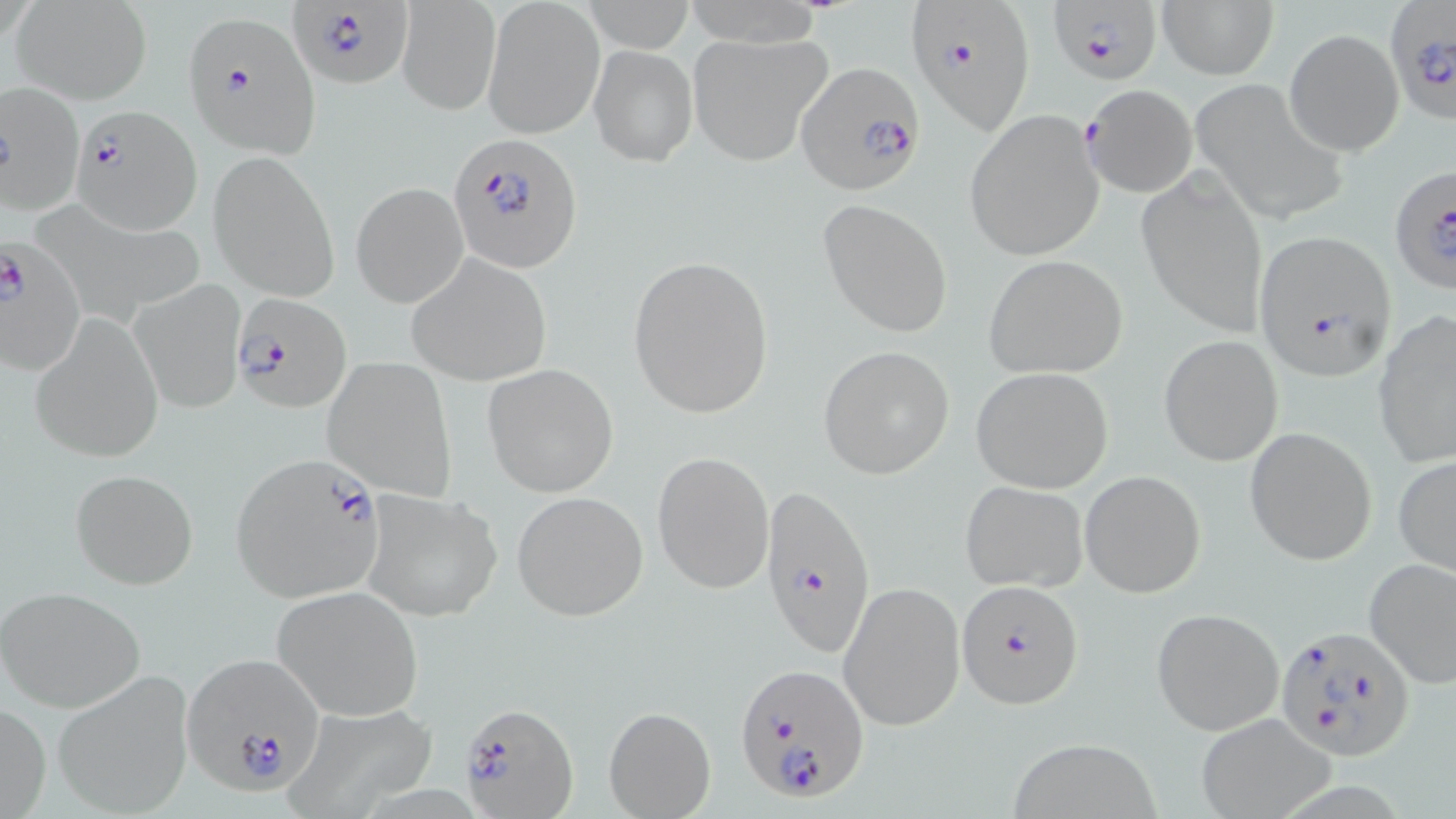 Approximate bounding boxes as (x1,y1)-(x2,y2) corner pairs in pixels. Plasmodium falciparum-infected red blood cell locations: (287,0)-(414,88), (902,0)-(1037,134), (1050,1)-(1161,84), (1384,3)-(1455,126), (182,10)-(320,157), (797,62)-(924,194), (0,82)-(84,214), (1081,84)-(1194,196), (70,106)-(200,232), (449,133)-(584,272), (1388,166)-(1456,295), (1251,230)-(1397,379), (0,234)-(86,375), (231,291)-(352,413), (228,454)-(389,603), (759,480)-(875,658), (957,582)-(1084,709), (1273,626)-(1418,760), (180,654)-(327,796), (735,663)-(868,802), (457,701)-(578,818). Uninfected red blood cell locations: (483,0)-(604,138), (681,0)-(827,48), (1157,1)-(1277,80), (12,2)-(152,105), (396,3)-(497,117), (1283,28)-(1404,155), (686,30)-(834,167), (588,44)-(697,166), (1192,78)-(1347,222), (963,108)-(1106,263), (210,149)-(340,303), (1137,168)-(1270,336), (351,182)-(468,308), (817,198)-(953,338), (406,254)-(553,384), (627,254)-(774,420), (983,254)-(1129,379), (130,278)-(246,412), (1373,309)-(1456,468), (28,313)-(163,462), (1158,334)-(1285,467), (817,345)-(955,479), (323,358)-(457,502), (483,364)-(621,497), (971,366)-(1115,493), (1244,426)-(1379,566), (651,451)-(774,593), (1394,455)-(1456,579), (1079,469)-(1206,597), (71,470)-(197,590), (960,481)-(1088,593), (358,487)-(503,623), (510,491)-(648,622), (1362,555)-(1456,689), (839,581)-(964,732), (271,586)-(425,718), (2,587)-(146,713), (1151,607)-(1284,736), (53,673)-(196,816), (277,701)-(440,817), (0,702)-(50,819), (604,706)-(716,819), (1191,711)-(1338,819), (1007,735)-(1161,818). Slide-level diagnosis: Plasmodium falciparum. One field of a larger specimen. Optical microscopy. May-Grünwald-Giemsa stain. Image is 1456×819 pixels. Thin blood film. 1000x magnification.